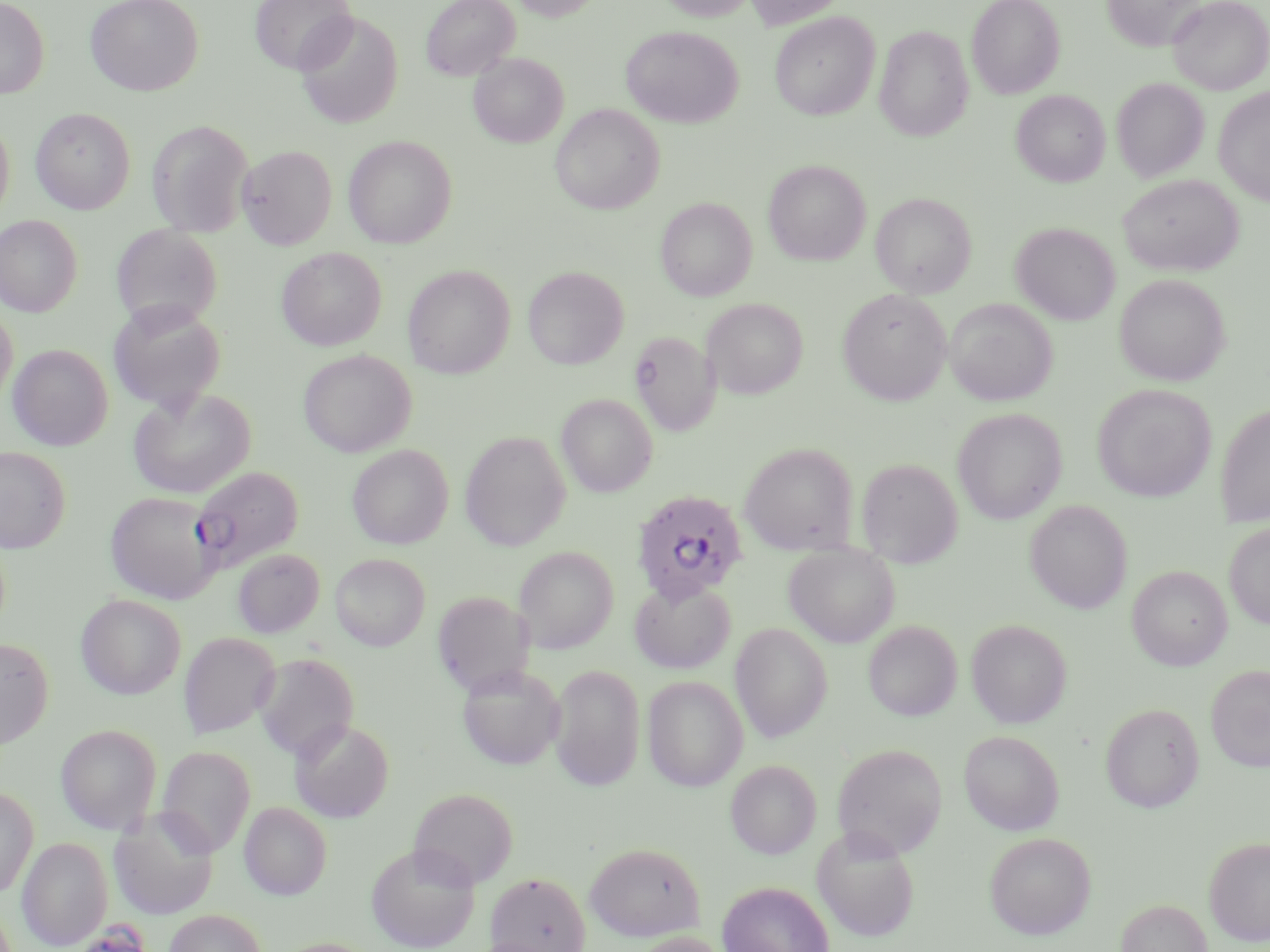
Approximate bounding boxes as (x1,y1)-(x2,y2) corner pairs in pixels. Uninfected red blood cell locations: (0,0)-(49,98), (85,0)-(204,96), (249,0)-(357,74), (421,0)-(520,81), (508,0)-(604,21), (657,0)-(756,21), (745,0)-(849,29), (967,0)-(1065,99), (1101,0)-(1205,52), (1167,0)-(1270,95), (295,11)-(403,129), (769,12)-(880,120), (874,25)-(974,142), (621,26)-(743,128), (469,52)-(568,148), (1111,78)-(1209,182), (1214,86)-(1270,206), (1011,90)-(1110,187), (550,103)-(664,214), (30,107)-(135,213), (0,115)-(14,224), (147,120)-(254,237), (343,135)-(457,248), (237,144)-(336,249), (763,160)-(871,265), (1117,174)-(1243,276), (870,192)-(977,298), (656,197)-(757,301), (0,215)-(82,317), (1011,222)-(1120,325), (110,224)-(223,330), (276,247)-(387,350), (402,265)-(515,378), (523,265)-(629,369), (1114,273)-(1231,386), (837,288)-(952,404), (702,298)-(808,399), (945,298)-(1057,405), (107,300)-(227,414), (0,305)-(18,408), (629,331)-(721,435), (8,344)-(113,450), (298,349)-(416,457), (1092,384)-(1216,502), (128,387)-(256,499), (556,393)-(658,497), (1215,402)-(1270,528), (952,407)-(1067,525), (459,431)-(571,551), (739,442)-(858,555), (347,444)-(453,549), (0,446)-(70,553), (856,457)-(963,567), (105,491)-(221,603), (1025,500)-(1132,613), (1223,522)-(1270,630), (784,544)-(900,647), (513,545)-(618,654), (232,549)-(324,638), (330,553)-(430,650), (1127,565)-(1232,671), (630,578)-(736,674), (432,590)-(536,696), (75,594)-(186,699), (966,619)-(1072,728), (864,621)-(962,721), (730,622)-(832,742), (179,631)-(280,738), (0,637)-(54,750), (254,652)-(359,761), (456,664)-(566,770), (1206,664)-(1270,772), (549,665)-(645,791), (642,675)-(747,791), (1101,702)-(1204,812), (290,719)-(394,822), (55,724)-(162,834), (958,730)-(1064,835), (831,743)-(947,859), (156,745)-(256,857), (725,760)-(821,859), (0,786)-(38,899), (409,787)-(518,887), (240,801)-(332,900), (109,808)-(219,920), (812,826)-(920,942), (984,831)-(1096,939), (1203,836)-(1270,946), (17,837)-(110,949), (365,842)-(481,952), (585,842)-(705,941), (486,871)-(591,952), (716,881)-(835,952), (1116,898)-(1212,952), (164,909)-(267,952), (626,931)-(730,952). Plasmodium falciparum-infected red blood cell locations: (190,466)-(303,572), (631,488)-(749,604). Slide-level diagnosis: Plasmodium falciparum. Captured at 1000x magnification. Image is 1270×952 pixels. May-Grünwald-Giemsa-stained preparation. Light microscopy. One field of a larger specimen. Thin blood smear.